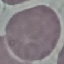

Summary:
  - Malaria status: uninfected
  - Stain: Giemsa
  - Capture: smartphone through the microscope eyepiece
  - Image type: cell patch, automatically extracted from a larger field of view and resized to 64 × 64 pixels
  - Preparation: thin blood smear